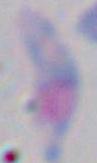

Summary:
  - Magnification: 1000x
  - Identification: Toxoplasma gondii
  - Modality: micrograph